Assess this cell for malaria.
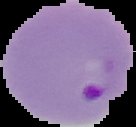
Parasitized.

Summary:
  - Preparation: thin blood smear
  - Image type: cell region segmented out of the field of view; surrounding area masked to black
  - Image size: 136×127 pixels